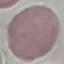
malaria status = uninfected
capture = smartphone camera at the microscope eyepiece
preparation = thin blood film
stain = Giemsa
image type = automatically extracted cell patch, resized to 64 × 64 pixels